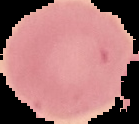
Summary:
  - Image size: 139×124 pixels
  - Preparation: thin blood smear
  - Result: negative for Plasmodium parasites
  - Image type: segmented cell region on a black background